Comment on the background quality.
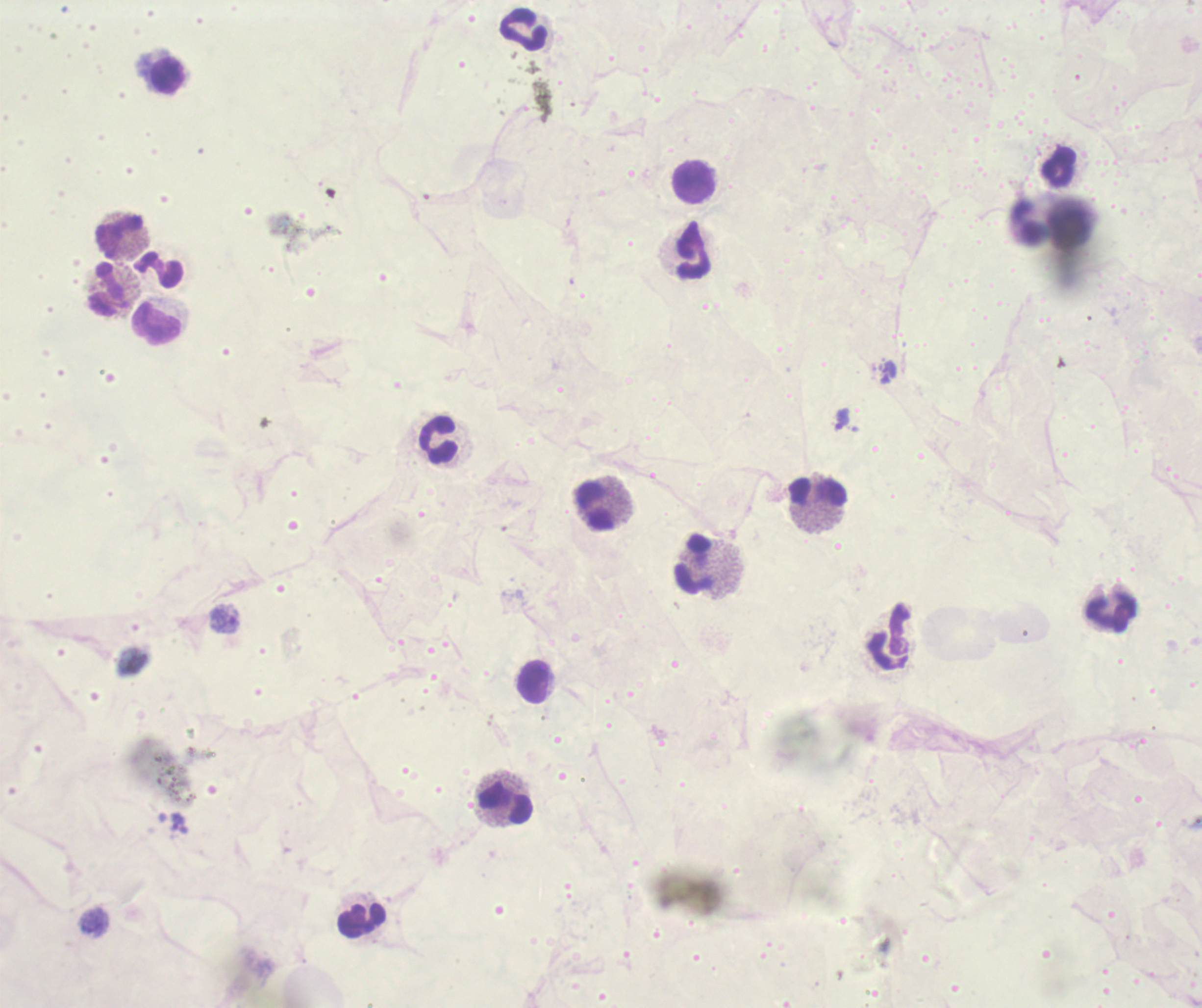
Unsatisfactory.

Approximate object centers, in pixels from the top-left corner. Trophozoite locations: (x=842, y=419), (x=225, y=618), (x=179, y=823). Leukocyte locations: (x=524, y=29), (x=167, y=76), (x=1060, y=165), (x=695, y=182), (x=1027, y=222), (x=120, y=236), (x=694, y=252), (x=158, y=268), (x=107, y=289), (x=155, y=323), (x=439, y=441), (x=817, y=493), (x=596, y=505), (x=695, y=564), (x=1110, y=612), (x=889, y=636), (x=534, y=682), (x=506, y=803), (x=360, y=921). Coloration quality: bad. Previously used in a real diagnosis. One field from this slide. Thick blood film. 100x magnification. Romanowsky-stained preparation. Result: Plasmodium parasites detected. Image is 1202×1008 pixels.